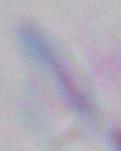
{
  "identification": "Toxoplasma gondii",
  "modality": "micrograph",
  "magnification": "1000x"
}